Assess the morphology of the erythrocytes.
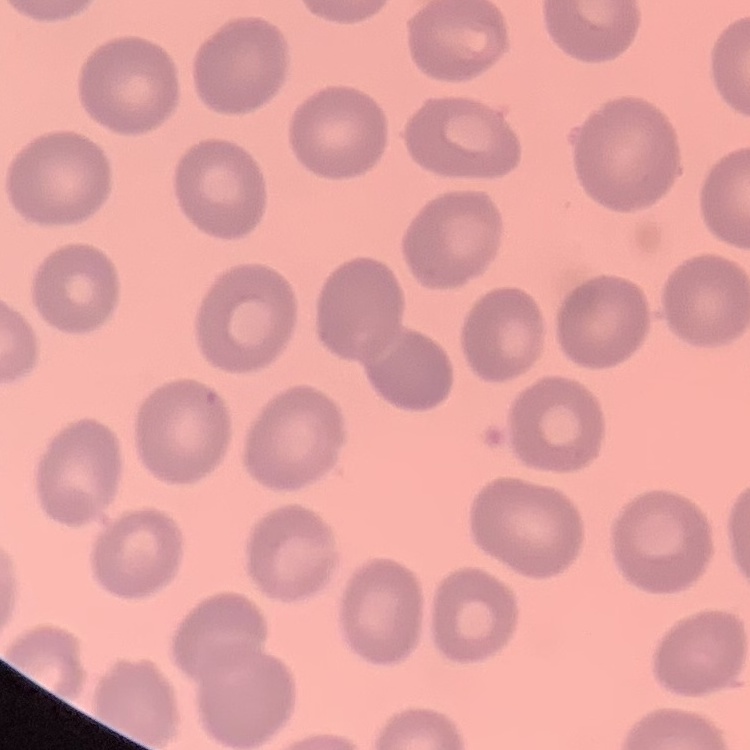

No rouleaux formation.

Summary:
  - Stain: Field's or Giemsa
  - Preparation: thin peripheral smear
  - Image type: one tile cut from a larger photomicrograph